State which parasite is depicted.
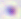

Toxoplasma gondii.

{
  "magnification": "400x",
  "modality": "photomicrograph"
}